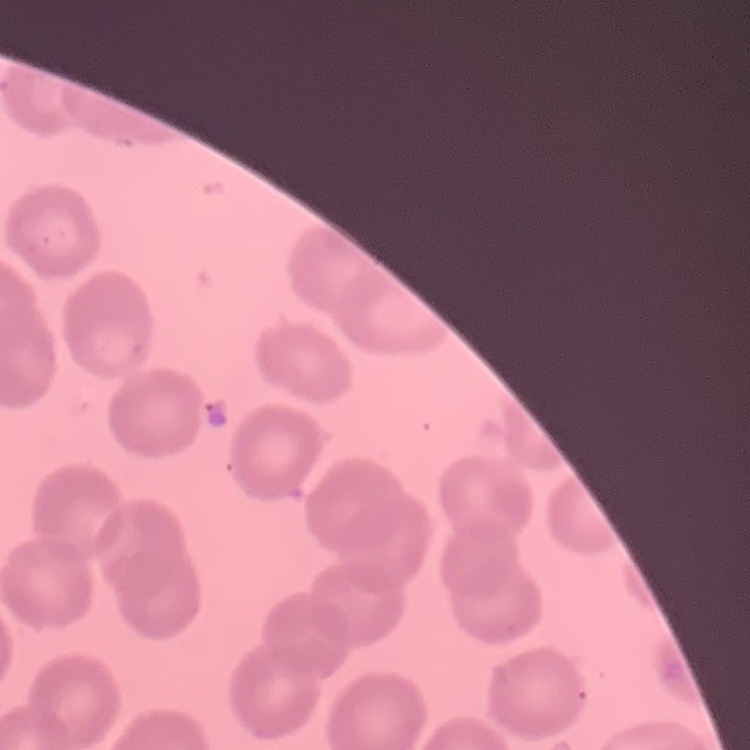
erythrocyte morphology = no rouleaux formation
preparation = thin blood film
stain = Field's or Giemsa
image type = one tile cut from a larger photomicrograph